Classify this cell by malaria status.
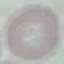
It is uninfected.

Cell patch, automatically extracted from a larger field of view and resized to 64 × 64 pixels. Thin blood smear. Giemsa stain. Photographed with a smartphone camera at the microscope eyepiece.